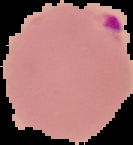

From a thin blood film. Image is 133×145 pixels. Malaria status: parasitized. The area outside the segmented cell region is set to black.